Assess this cell for malaria.
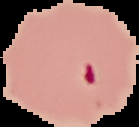
It is parasitized.

{
  "preparation": "thin blood smear",
  "image_size": "139×127 pixels",
  "image_type": "cell region segmented out of the field of view; surrounding area masked to black"
}